Outline each blood parasite and name the species.
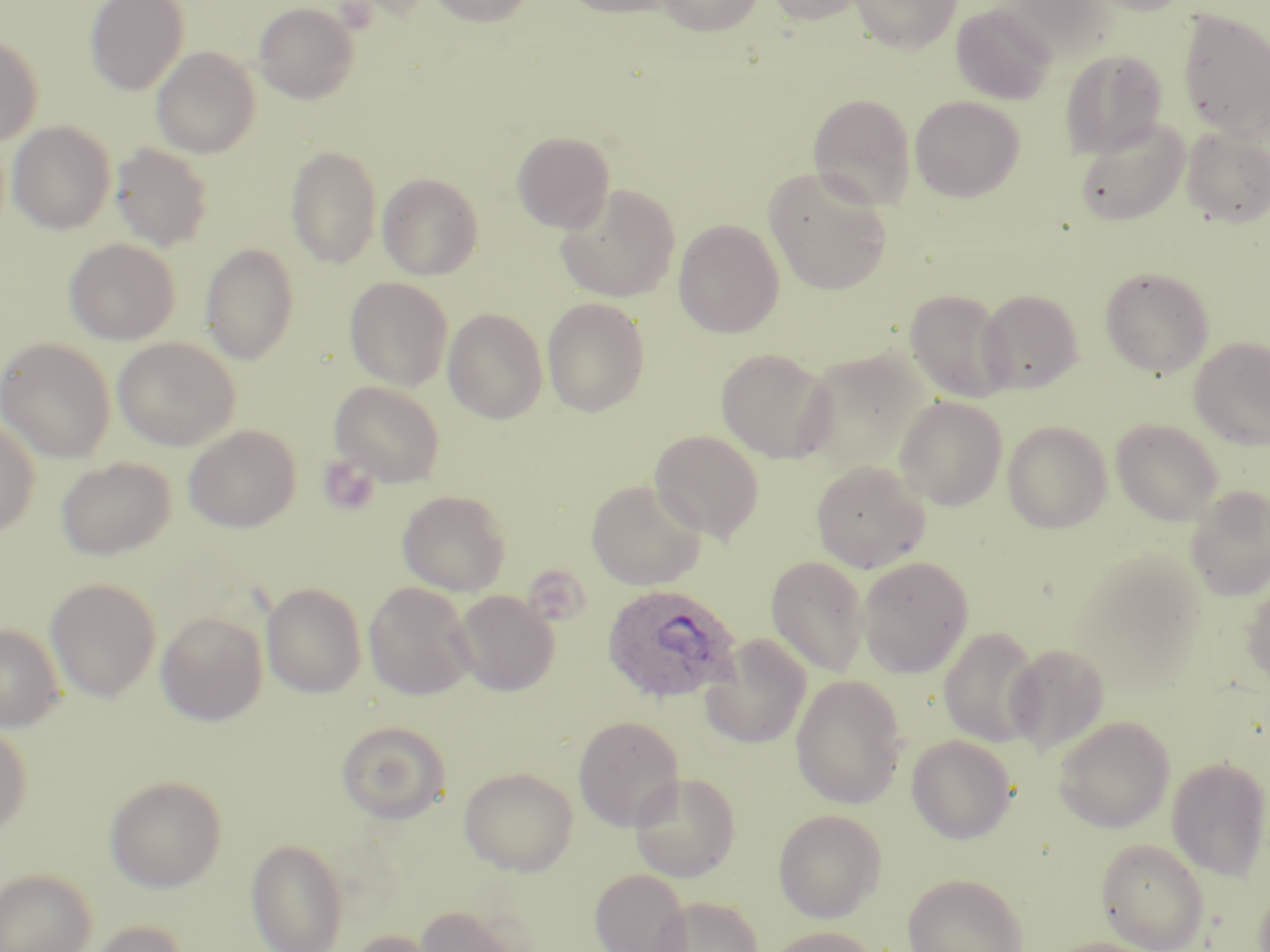

Approximate bounding boxes as [x1, y1, x2, y2] in pixels.
Plasmodium ovale-infected red blood cells: [601, 582, 739, 706].
No Plasmodium falciparum, Plasmodium malariae, Plasmodium vivax, Babesia divergens, or Trypanosoma brucei observed.

Summary:
  - Uninfected red blood cell locations: [85, 0, 189, 95], [428, 0, 535, 27], [560, 0, 679, 19], [656, 0, 764, 35], [765, 0, 869, 26], [850, 0, 960, 52], [1083, 0, 1193, 16], [253, 2, 360, 104], [950, 3, 1057, 106], [1178, 9, 1270, 141], [0, 34, 43, 147], [151, 47, 260, 158], [1060, 49, 1169, 157], [808, 93, 916, 211], [909, 95, 1025, 202], [1075, 118, 1191, 227], [7, 121, 116, 234], [1181, 128, 1270, 227], [512, 131, 615, 233], [111, 143, 214, 252], [285, 145, 382, 268], [764, 168, 892, 295], [377, 173, 484, 280], [555, 183, 681, 303], [673, 219, 784, 338], [65, 238, 180, 345], [200, 243, 300, 365], [1100, 266, 1215, 378], [345, 277, 453, 390], [904, 289, 1014, 403], [977, 289, 1083, 394], [542, 297, 650, 417], [443, 308, 548, 424], [1189, 336, 1270, 449], [0, 337, 116, 463], [112, 337, 240, 451], [716, 348, 835, 464], [798, 349, 931, 473], [330, 381, 446, 487], [895, 396, 1008, 510], [0, 415, 40, 538], [1111, 418, 1224, 525], [1002, 420, 1112, 534], [184, 425, 301, 533], [649, 429, 765, 543], [56, 457, 176, 560], [810, 459, 932, 573], [586, 480, 707, 590], [1185, 487, 1270, 602], [397, 489, 512, 597], [1071, 548, 1209, 690], [765, 555, 870, 678], [858, 556, 974, 678], [1242, 576, 1270, 687], [45, 578, 161, 702], [261, 582, 367, 698], [363, 582, 477, 701], [452, 590, 560, 696], [156, 611, 267, 725], [0, 623, 65, 732], [938, 625, 1043, 747], [701, 633, 813, 750], [1004, 643, 1110, 756], [791, 674, 907, 809], [573, 715, 685, 831], [1052, 716, 1175, 833], [335, 721, 452, 824], [0, 723, 32, 838], [906, 735, 1017, 843], [1165, 755, 1270, 880], [459, 767, 578, 876], [629, 772, 742, 882], [105, 774, 228, 892], [773, 809, 886, 922], [246, 838, 348, 952], [1096, 838, 1210, 952], [0, 868, 97, 952], [590, 868, 692, 952], [902, 872, 1029, 952], [1251, 882, 1270, 949], [653, 897, 764, 952], [414, 904, 530, 952], [82, 919, 190, 952], [765, 926, 882, 952], [343, 929, 443, 952], [1043, 937, 1166, 952]
  - Platelet locations: [317, 455, 381, 517]
  - Slide-level diagnosis: Plasmodium ovale
  - Modality: light microscopy
  - Stain: May-Grünwald-Giemsa
  - Magnification: 1000x
  - Preparation: thin blood film
  - Field of view: single
  - Image size: 1270×952 pixels